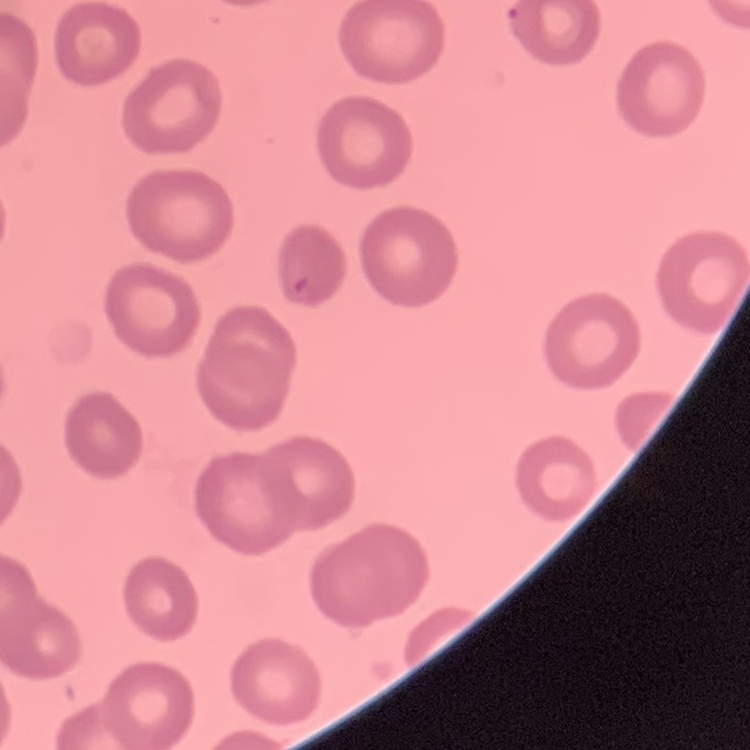
red blood cell morphology = no rouleaux formation
image type = one tile cut from a larger photomicrograph
stain = Field's or Giemsa
preparation = thin blood film